Name the cell type shown.
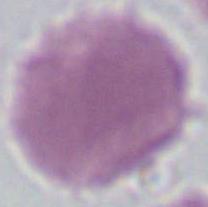

This is an erythrocyte.

modality: micrograph
magnification: 1000x